Assess this cell for malaria.
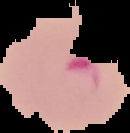
Parasitized.

image size = 130×133 pixels
image type = segmented cell region on a black background
preparation = thin blood film